Comment on the morphology of the erythrocytes.
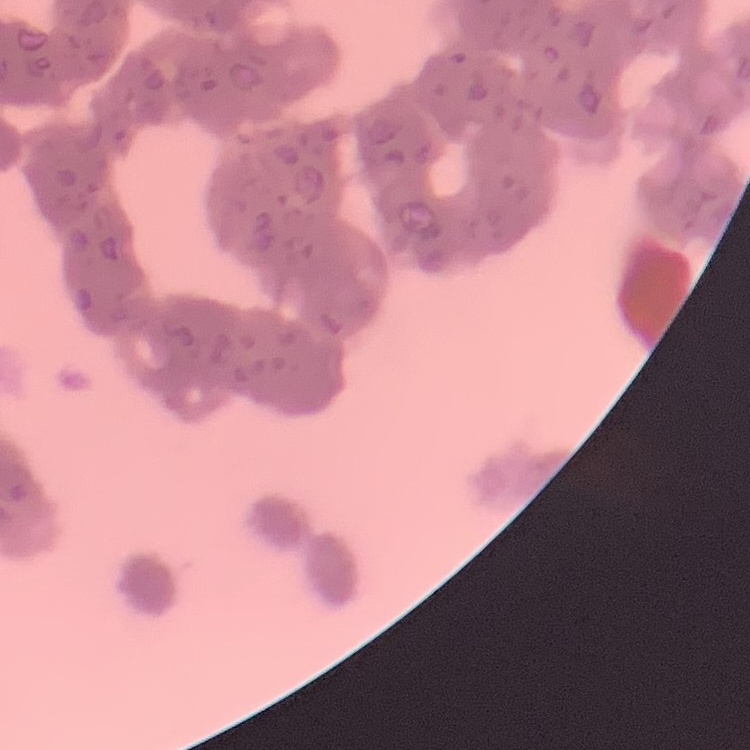

Rouleaux formation.

One tile cut from a larger photomicrograph. Stained with either Field's or Giemsa. Thin peripheral smear.